Report the malaria status of this cell.
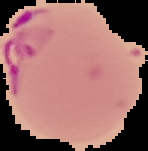
It is parasitized.

Summary:
  - Preparation: thin blood film
  - Image size: 148×151 pixels
  - Image type: segmented cell region on a black background